Assess for malaria.
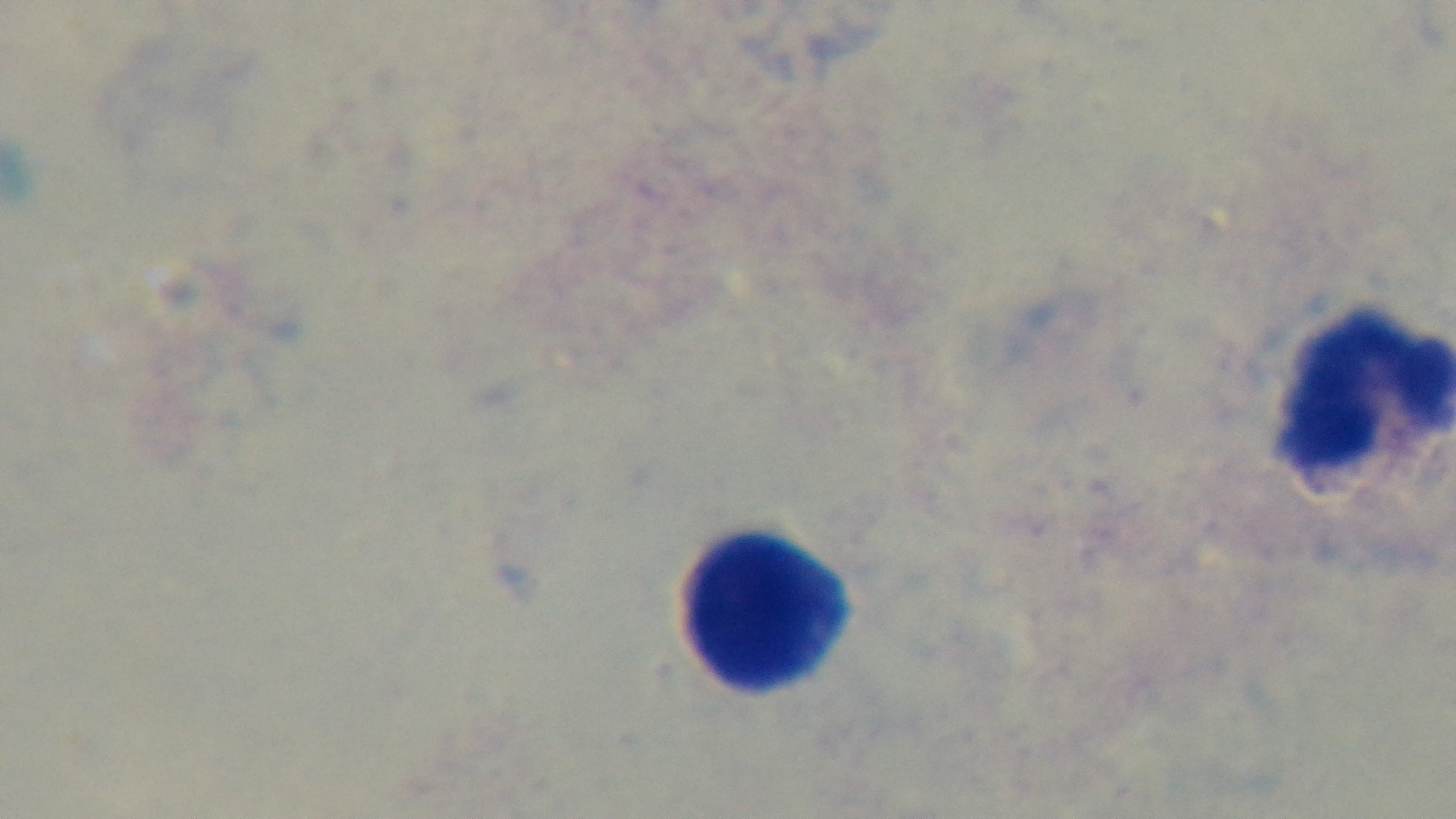

Negative.

field of view = single
objective = 100x oil immersion
capture = mounted 4K digital camera
preparation = thick
stain = Giemsa
modality = light microscopy